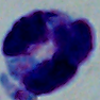

Summary:
  - Magnification: 1000x
  - Modality: photomicrograph
  - Identification: leukocyte